Describe the morphology of the erythrocytes.
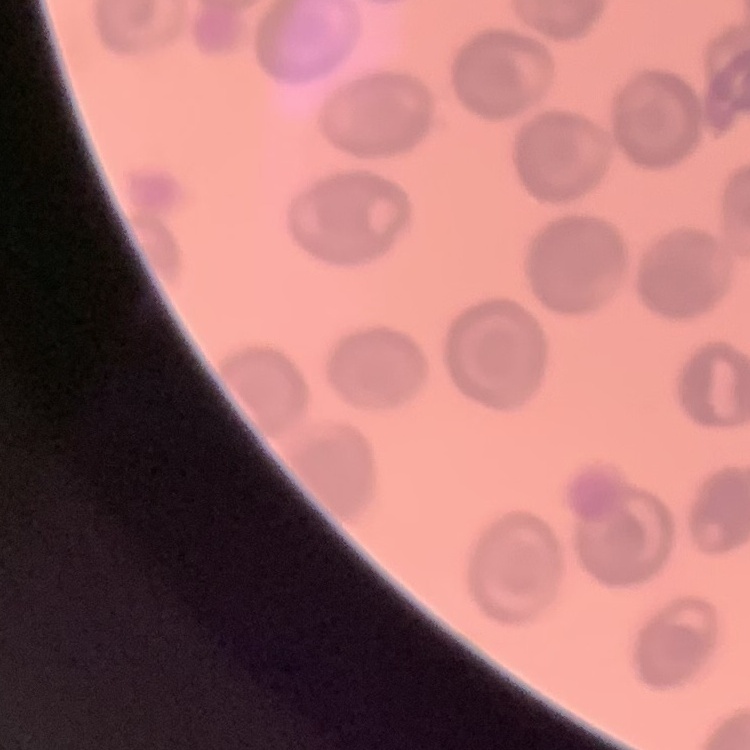

They show no rouleaux formation.

Square crop of a larger photomicrograph. Stained with either Field's or Giemsa. Thin peripheral smear.